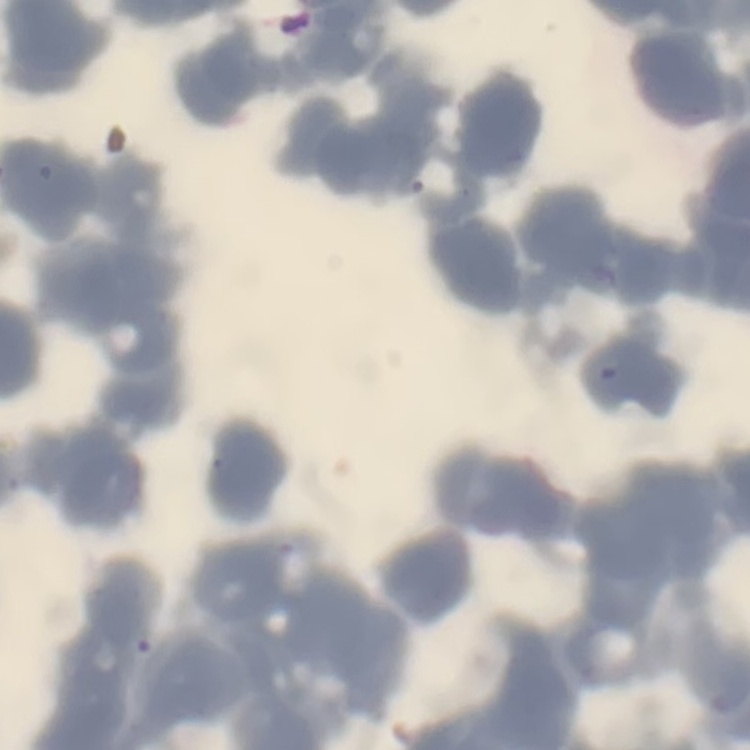

Summary:
  - Red blood cell morphology: rouleaux formation
  - Image type: square crop of a larger photomicrograph
  - Stain: Field's or Giemsa
  - Preparation: thin blood film